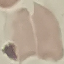
Summary:
  - Result: no malaria parasites detected
  - Preparation: thin smear
  - Image type: cell patch, automatically extracted from a larger field of view and resized to 64 × 64 pixels
  - Capture: smartphone camera at the microscope eyepiece
  - Stain: Giemsa